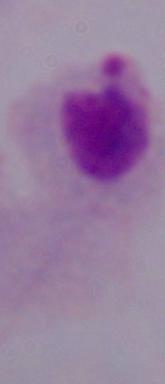

Summary:
  - Magnification: 1000x
  - Identification: trichomonad
  - Modality: photomicrograph